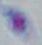 Captured at 1000x magnification. Toxoplasma gondii is shown. Micrograph.